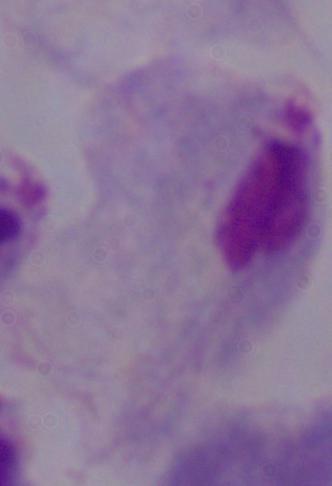
{
  "identification": "trichomonad",
  "modality": "photomicrograph",
  "magnification": "1000x"
}